Identify the parasite.
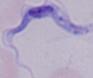
This is a trypanosome.

Summary:
  - Modality: micrograph
  - Magnification: 1000x